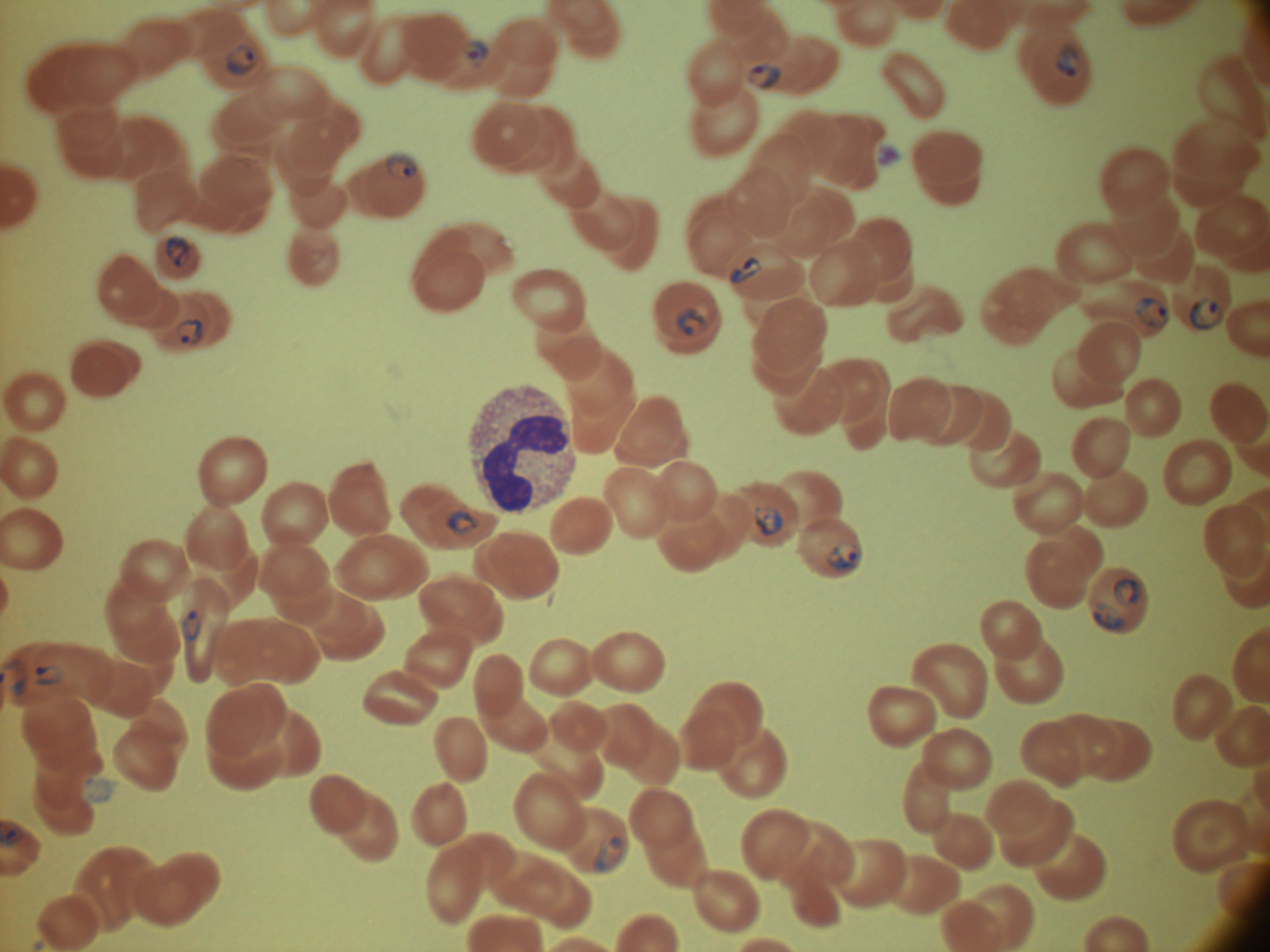

Approximate bounding boxes as named x1/y1/x2/y2 corners in pixels, from the source annotation, which is not necessarily exhaustive.
Summary:
  - Ring form locations: (x1=463, y1=40, x2=488, y2=68), (x1=1055, y1=43, x2=1080, y2=78), (x1=227, y1=45, x2=259, y2=76), (x1=748, y1=63, x2=782, y2=91), (x1=385, y1=151, x2=419, y2=181), (x1=166, y1=236, x2=191, y2=267), (x1=730, y1=256, x2=762, y2=285), (x1=1134, y1=297, x2=1168, y2=329), (x1=1190, y1=299, x2=1221, y2=330), (x1=676, y1=307, x2=707, y2=338), (x1=176, y1=319, x2=204, y2=345), (x1=753, y1=506, x2=782, y2=536), (x1=445, y1=509, x2=478, y2=536), (x1=827, y1=542, x2=862, y2=570), (x1=1113, y1=579, x2=1139, y2=607), (x1=1094, y1=602, x2=1124, y2=631), (x1=182, y1=610, x2=201, y2=642), (x1=35, y1=664, x2=63, y2=686), (x1=592, y1=835, x2=628, y2=874)
  - Field of view: single
  - Species: Plasmodium falciparum
  - Image size: 1270×952 pixels
  - Preparation: thin blood film
  - Magnification: 100x
  - Stain: Giemsa
  - Microscope: Leica DM2000 with built-in camera